Identify the cell.
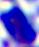
A leukocyte.

Summary:
  - Modality: photomicrograph
  - Magnification: 400x